Classify this cell by malaria status.
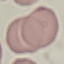
Uninfected.

Summary:
  - Capture: smartphone through the microscope eyepiece
  - Image type: automatically extracted cell patch, resized to 64 × 64 pixels
  - Preparation: thin blood film
  - Stain: Giemsa